State which cell type is depicted.
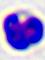

A leukocyte.

Micrograph. 400x magnification.